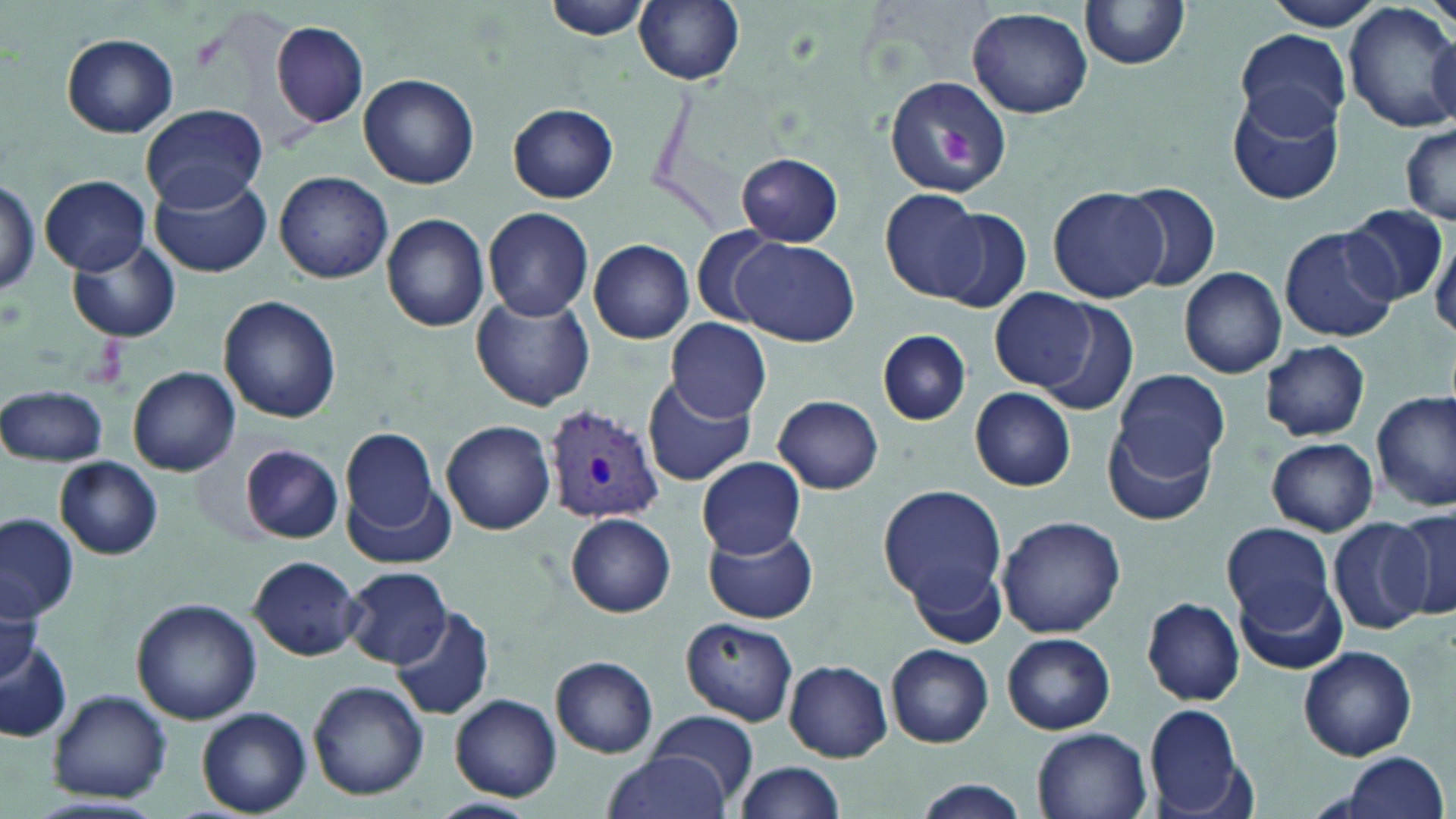

Summary:
  - Coordinate format: approximate bounding boxes as (x1, y1, x2, y2) in pixels
  - Uninfected red blood cell locations: (543, 0, 655, 41), (634, 0, 746, 85), (1079, 0, 1193, 70), (1263, 0, 1389, 33), (1345, 4, 1456, 133), (966, 6, 1093, 118), (270, 20, 370, 129), (1234, 32, 1348, 134), (60, 33, 179, 138), (358, 73, 480, 188), (884, 73, 1012, 197), (1226, 90, 1345, 207), (141, 105, 268, 209), (508, 105, 618, 203), (1400, 123, 1455, 225), (736, 152, 844, 245), (149, 170, 272, 277), (275, 170, 393, 284), (40, 175, 151, 274), (1, 179, 41, 299), (1118, 181, 1224, 293), (1047, 186, 1169, 303), (880, 188, 990, 304), (1343, 204, 1448, 305), (482, 206, 594, 321), (936, 207, 1032, 313), (380, 213, 492, 333), (1279, 225, 1399, 343), (691, 226, 785, 327), (1428, 227, 1456, 335), (66, 238, 182, 344), (733, 238, 858, 345), (588, 239, 695, 344), (1179, 267, 1286, 378), (991, 290, 1096, 390), (471, 294, 594, 412), (218, 296, 339, 425), (1034, 302, 1138, 417), (665, 318, 772, 421), (879, 331, 970, 425), (1260, 340, 1370, 441), (127, 366, 241, 476), (644, 371, 756, 487), (1115, 371, 1230, 484), (0, 383, 108, 467), (969, 387, 1077, 491), (1373, 390, 1456, 511), (772, 396, 884, 494), (441, 420, 556, 535), (1104, 423, 1216, 526), (341, 429, 439, 535), (1265, 437, 1378, 536), (240, 444, 343, 544), (55, 456, 163, 561), (697, 456, 806, 557), (346, 479, 458, 570), (876, 484, 1007, 616), (1388, 506, 1456, 624), (0, 513, 78, 623), (565, 513, 677, 617), (998, 515, 1128, 639), (1326, 518, 1434, 634), (1222, 520, 1336, 632), (704, 524, 818, 624), (248, 556, 363, 660), (342, 567, 451, 669), (1238, 580, 1347, 675), (0, 589, 43, 683), (1141, 597, 1244, 705), (131, 598, 261, 724), (390, 606, 497, 723), (679, 616, 799, 727), (1002, 633, 1115, 734), (0, 636, 74, 743), (886, 644, 994, 748), (1298, 646, 1417, 761), (551, 656, 659, 758), (784, 659, 893, 761), (308, 679, 428, 800), (47, 689, 171, 804), (450, 693, 562, 801), (1142, 704, 1249, 818), (196, 707, 313, 817), (650, 709, 761, 805), (1032, 727, 1153, 819), (599, 751, 732, 819), (1328, 752, 1450, 819), (735, 761, 845, 816), (911, 780, 1032, 816), (430, 795, 537, 817)
  - Plasmodium vivax-infected red blood cell locations: (543, 403, 665, 525)
  - Platelet locations: (931, 127, 977, 164)
  - Slide-level diagnosis: Plasmodium vivax
  - Image size: 1456×819 pixels
  - Preparation: thin blood smear
  - Field of view: single
  - Magnification: 1000x
  - Stain: May-Grünwald-Giemsa
  - Modality: optical microscopy